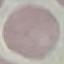

Result: no malaria parasites seen. Thin blood film. Acquired by smartphone through the microscope eyepiece. Giemsa stain. Automatically extracted cell patch, resized to 64 × 64 pixels.